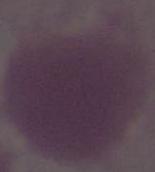

{
  "identification": "erythrocyte",
  "magnification": "1000x",
  "modality": "micrograph"
}